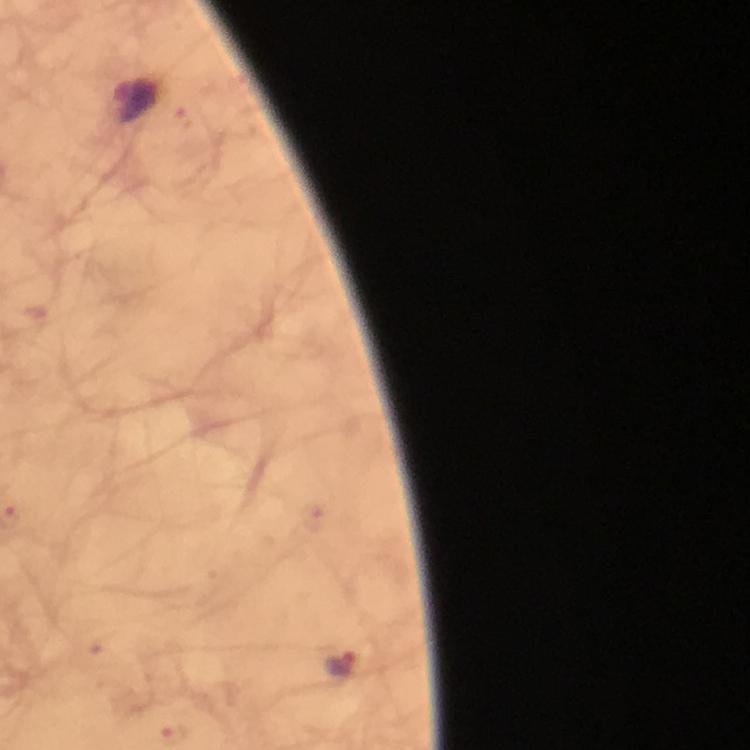
Approximate object centers, in pixels from the top-left corner.
Summary:
  - Malaria parasite locations: (x=183, y=119), (x=340, y=663)
  - Preparation: thick blood film
  - Image size: 750×750 pixels
  - Cropped from: a single field of view
  - Stain: Giemsa
  - Immersion oil: used
  - Magnification: 100x
  - Context: from a malaria diagnostic workup
  - Capture: smartphone photograph through a microscope